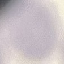
Summary:
  - Result: no malaria parasites detected
  - Stain: Giemsa
  - Capture: smartphone through the microscope eyepiece
  - Image type: automatically extracted cell patch, resized to 64 × 64 pixels
  - Preparation: thin smear